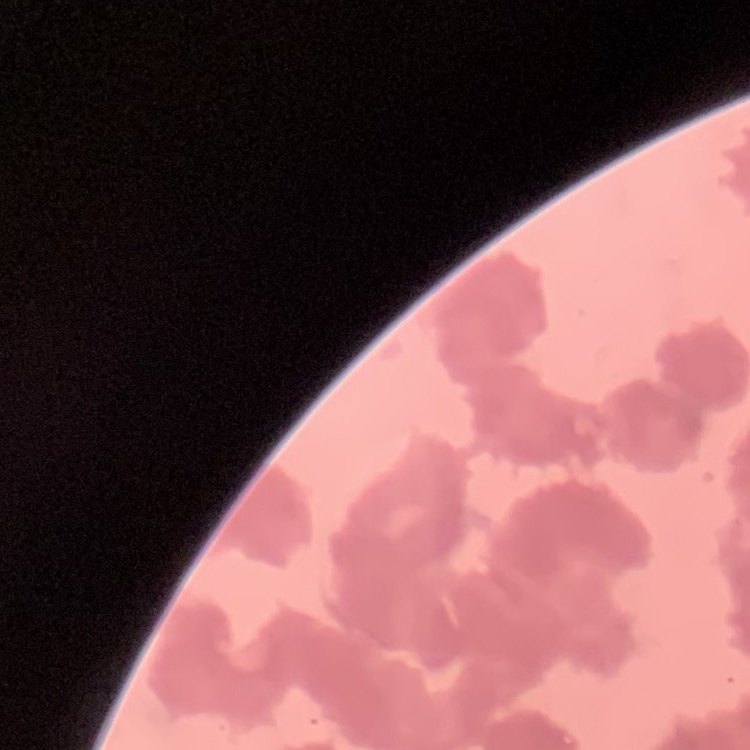 The red blood cells exhibit rouleaux formation. Square crop of a larger photomicrograph. Field's or Giemsa stain. Thin blood film.